Classify this cell by malaria status.
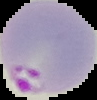

Parasitized.

image size = 97×100 pixels
image type = segmented cell region with the area outside set to black
preparation = thin blood film